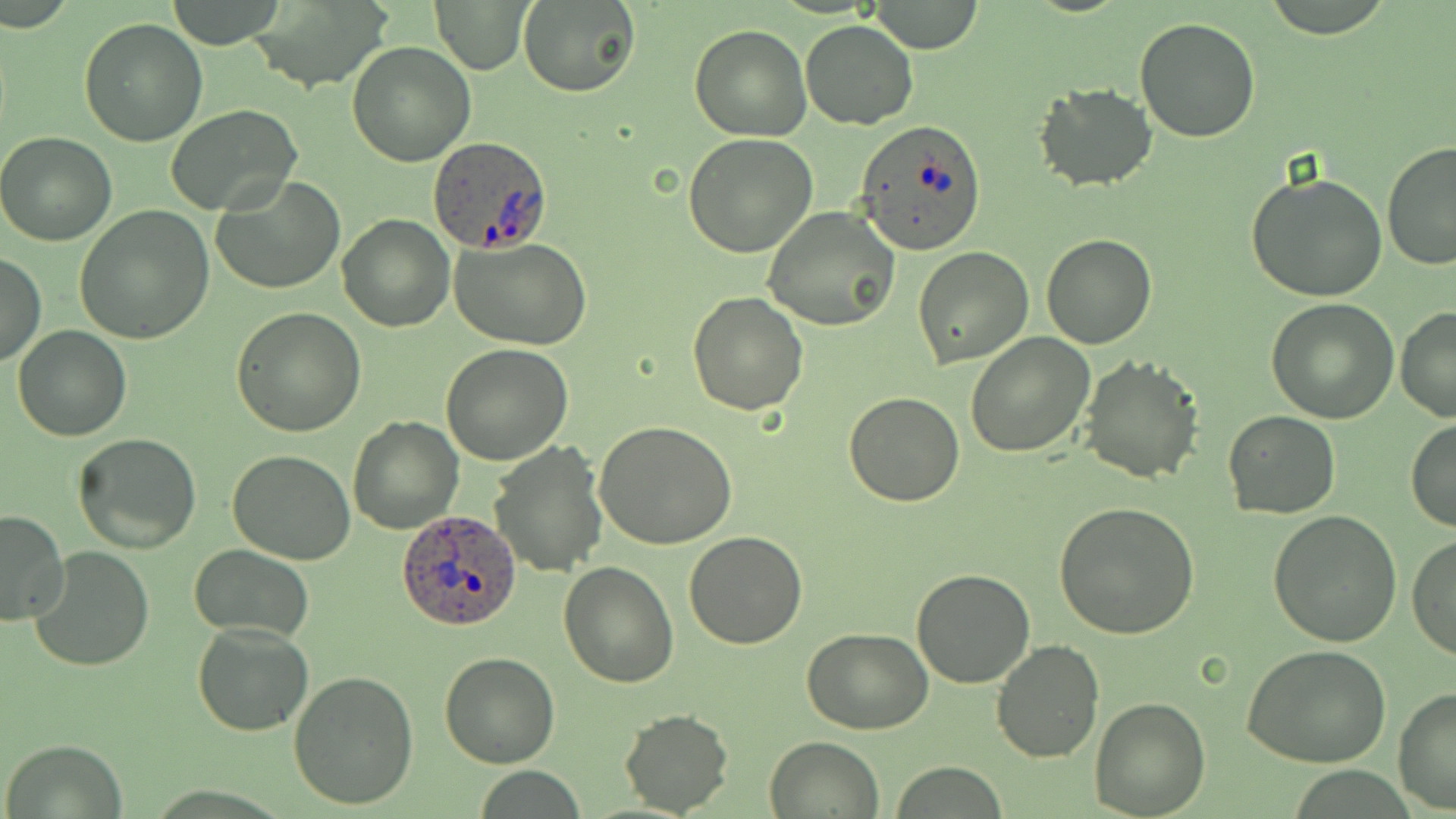

Approximate bounding boxes as (x1,y1)-(x2,y2) corner pairs in pixels. Plasmodium ovale-infected red blood cell locations: (855,119)-(987,254), (426,136)-(551,252), (398,508)-(523,633). Uninfected red blood cell locations: (166,0)-(287,48), (518,0)-(639,97), (868,0)-(985,53), (242,1)-(394,93), (432,1)-(529,74), (1132,17)-(1260,142), (78,18)-(208,147), (800,20)-(919,130), (690,25)-(811,141), (347,42)-(476,166), (1034,83)-(1157,192), (165,104)-(302,217), (0,132)-(116,247), (682,134)-(818,259), (1381,140)-(1456,269), (1246,172)-(1390,302), (213,175)-(345,294), (75,205)-(213,343), (762,207)-(899,332), (337,213)-(454,332), (1042,233)-(1157,349), (451,239)-(592,350), (913,247)-(1033,368), (0,253)-(45,367), (687,291)-(809,417), (1267,299)-(1400,424), (1396,304)-(1455,421), (232,306)-(367,437), (12,326)-(131,441), (966,333)-(1096,458), (440,345)-(572,465), (1077,356)-(1203,482), (844,393)-(965,508), (1223,411)-(1340,518), (348,416)-(464,533), (1407,419)-(1456,532), (594,421)-(739,550), (73,433)-(201,551), (490,438)-(608,576), (227,450)-(355,564), (1053,502)-(1200,639), (0,509)-(69,627), (1268,510)-(1404,647), (683,531)-(807,649), (1408,535)-(1456,662), (188,545)-(313,639), (28,546)-(155,673), (557,561)-(680,686), (911,569)-(1036,688), (190,621)-(314,736), (802,627)-(933,732), (990,639)-(1104,763), (1245,644)-(1395,770), (440,651)-(561,769), (288,671)-(420,811), (1392,687)-(1456,812), (1089,697)-(1210,817), (620,709)-(734,816), (765,735)-(885,818), (3,739)-(128,817), (891,763)-(1008,817). Slide-level diagnosis: Plasmodium ovale. Single field of view. May-Grünwald-Giemsa-stained preparation. Light microscopy. Thin blood film. Image is 1456×819 pixels. 1000x magnification.